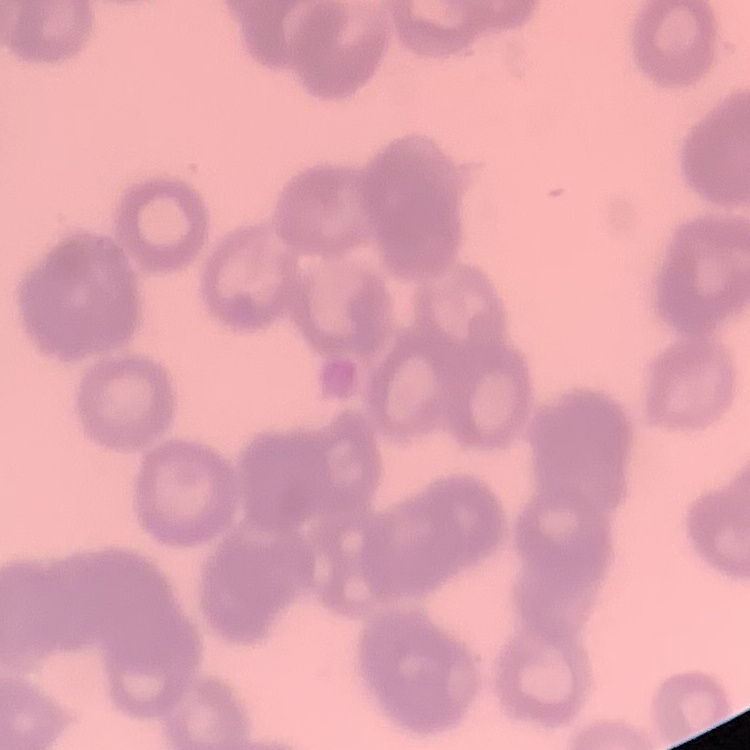

The red blood cells exhibit rouleaux formation. Square crop of a larger photomicrograph. Stained with either Field's or Giemsa. Thin blood film.